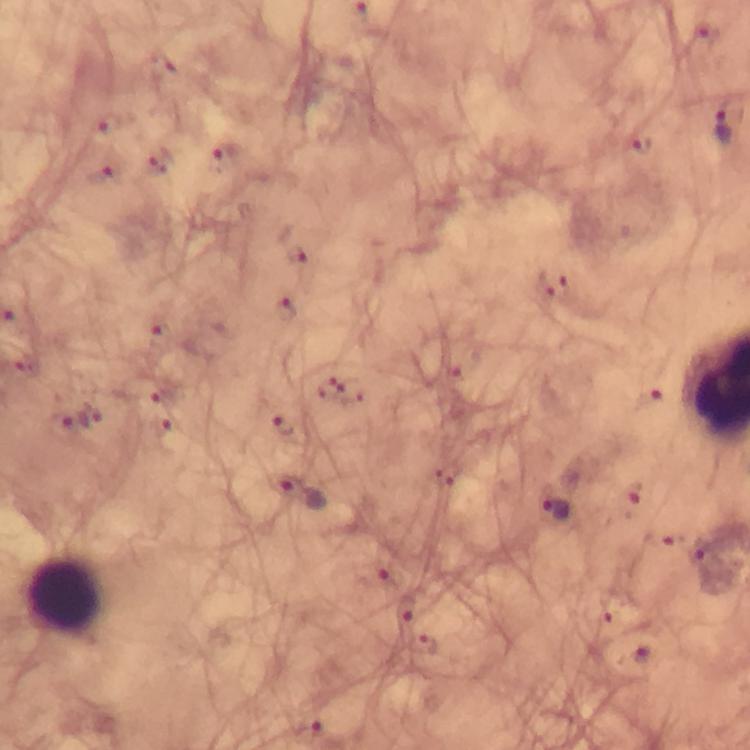

Approximate object centers, in pixels from the top-left corner. Leukocyte locations: (x=64, y=596). Malaria parasite locations: (x=706, y=37), (x=726, y=123), (x=108, y=128), (x=641, y=146), (x=223, y=161), (x=156, y=162), (x=104, y=173), (x=298, y=254), (x=551, y=283), (x=286, y=310), (x=161, y=324), (x=324, y=387), (x=352, y=391), (x=163, y=397), (x=643, y=398), (x=90, y=417), (x=60, y=424), (x=285, y=425), (x=162, y=428), (x=297, y=492), (x=633, y=492), (x=558, y=510), (x=704, y=558), (x=389, y=575), (x=405, y=613), (x=427, y=646), (x=312, y=729). Thick blood film. Giemsa-stained preparation. Immersion oil was used. Image is 750×750 pixels. A crop from one field of view. 100x magnification. Photographed through the microscope with a smartphone camera. From a diagnostic examination for malaria.